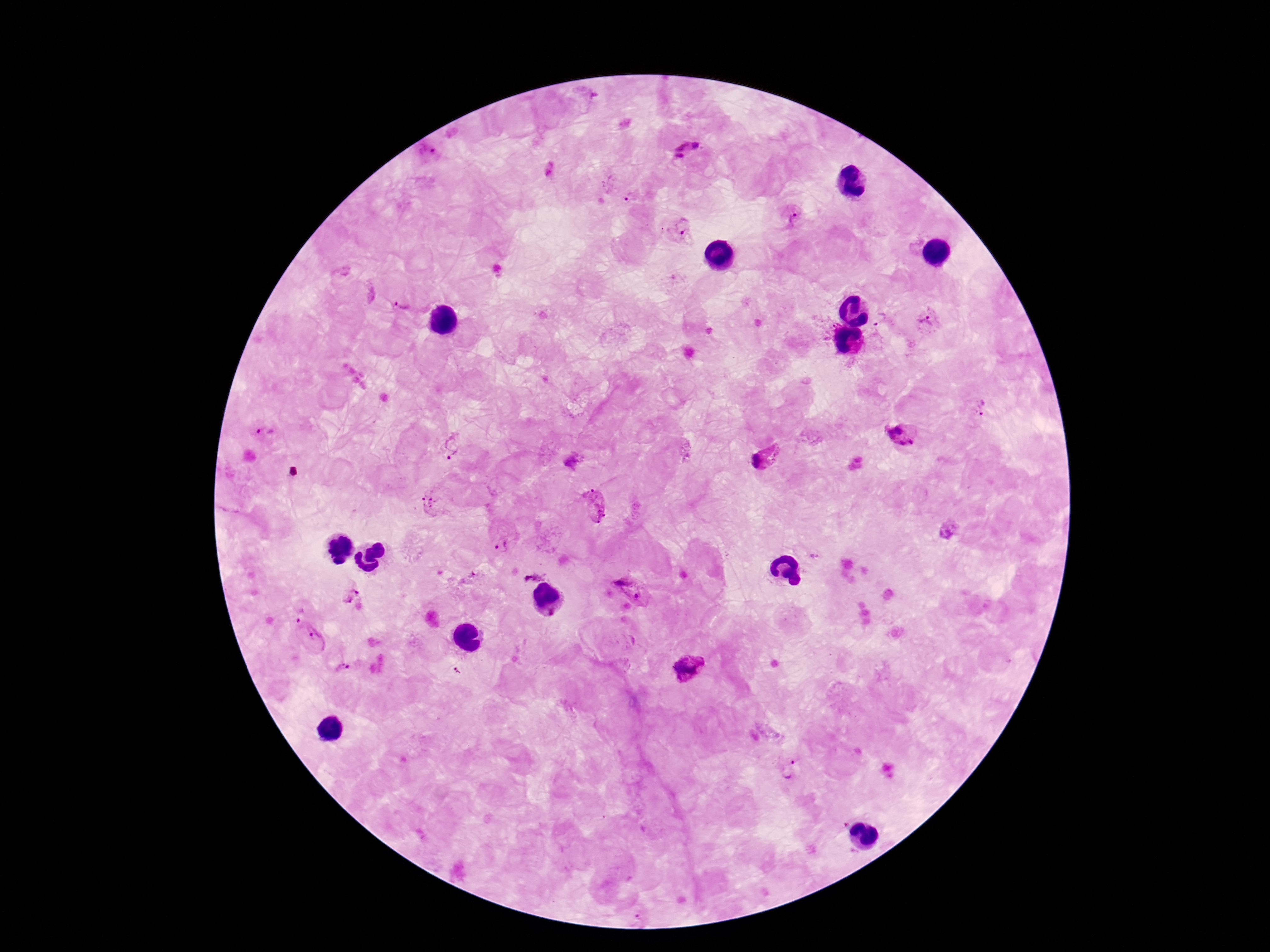 Approximate object centers, in pixels from the top-left corner. Plasmodium parasite locations: (x=688, y=150), (x=430, y=153), (x=633, y=200), (x=792, y=216), (x=679, y=232), (x=402, y=307), (x=929, y=324), (x=983, y=409), (x=263, y=431), (x=901, y=433), (x=452, y=445), (x=767, y=457), (x=433, y=502), (x=595, y=503), (x=949, y=529), (x=499, y=546), (x=814, y=556), (x=532, y=573), (x=629, y=588), (x=349, y=595), (x=297, y=614), (x=317, y=643), (x=345, y=668), (x=687, y=669), (x=456, y=671), (x=792, y=771). Giemsa-stained preparation. Patient malaria status: positive. 100x magnification. Single field of view. Thick blood smear. Smartphone photograph taken through the microscope eyepiece. Image is 1270×952 pixels.